Point out each leukocyte.
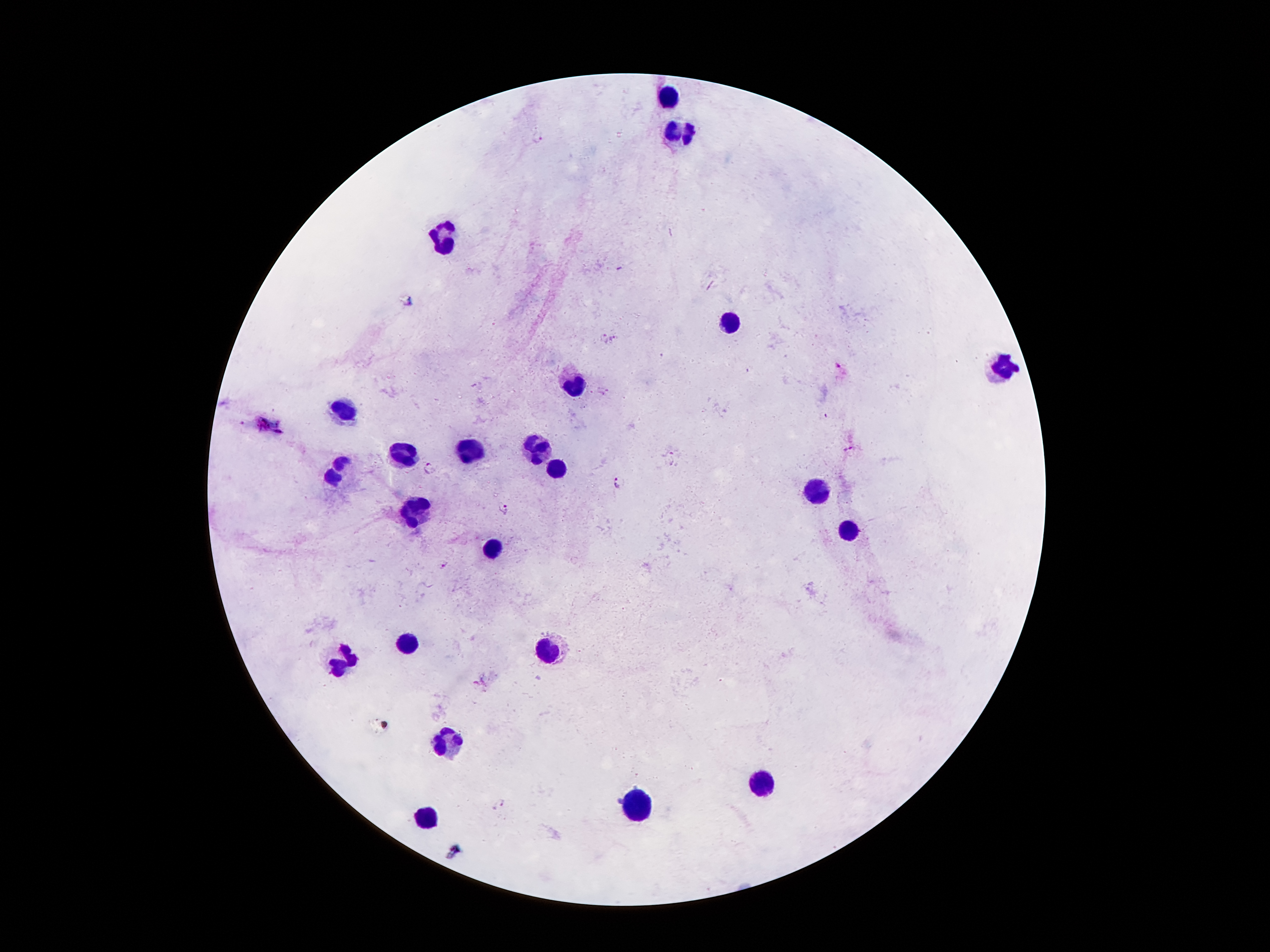
Approximate centers as {x, y} in pixels.
Leukocytes: {668, 97}, {679, 130}, {447, 240}, {734, 322}, {1004, 368}, {573, 384}, {349, 408}, {537, 448}, {469, 450}, {407, 452}, {557, 468}, {336, 472}, {816, 488}, {420, 514}, {849, 530}, {491, 549}, {409, 649}, {546, 651}, {444, 737}, {760, 784}, {639, 806}, {424, 821}.

Malaria parasite locations: {536, 135}, {602, 338}, {614, 338}, {823, 415}, {848, 449}, {672, 458}, {430, 467}, {616, 481}, {503, 508}, {442, 564}, {498, 803}. Photographed through the microscope eyepiece with a smartphone camera. Patient malaria status: positive for Plasmodium falciparum. Thick blood film. 100x magnification. Single field of view. Giemsa stain. Image is 1270×952 pixels.